Mark where leukocytes are.
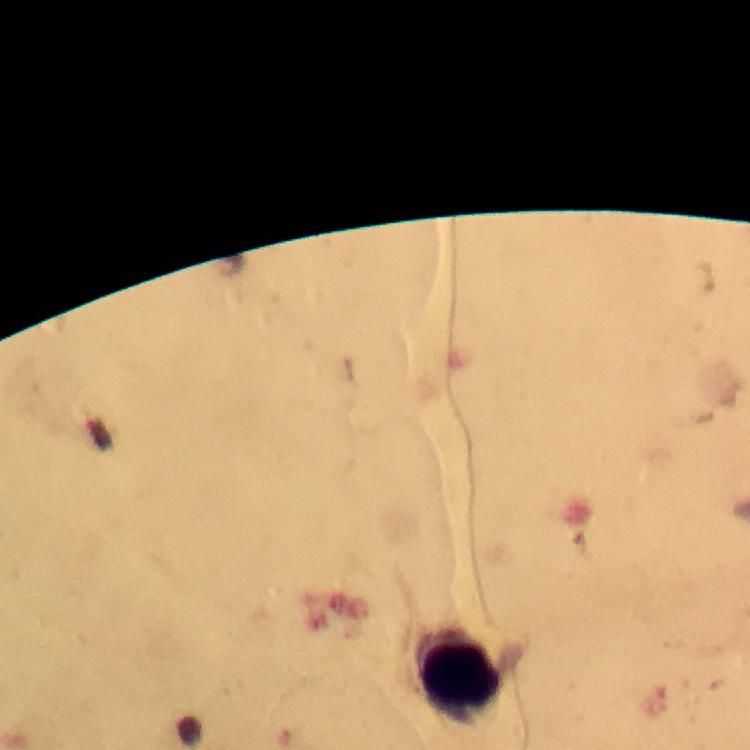

Approximate object centers, in pixels from the top-left corner.
Leukocytes: (x=460, y=676).

immersion_oil: used
plasmodium_parasites: none detected
cropped_from: a single field of view
capture: smartphone camera through the microscope
stain: Giemsa
image_size: 750×750 pixels
magnification: 100x
context: from a malaria diagnostic workup
preparation: thick blood smear